Report the malaria status.
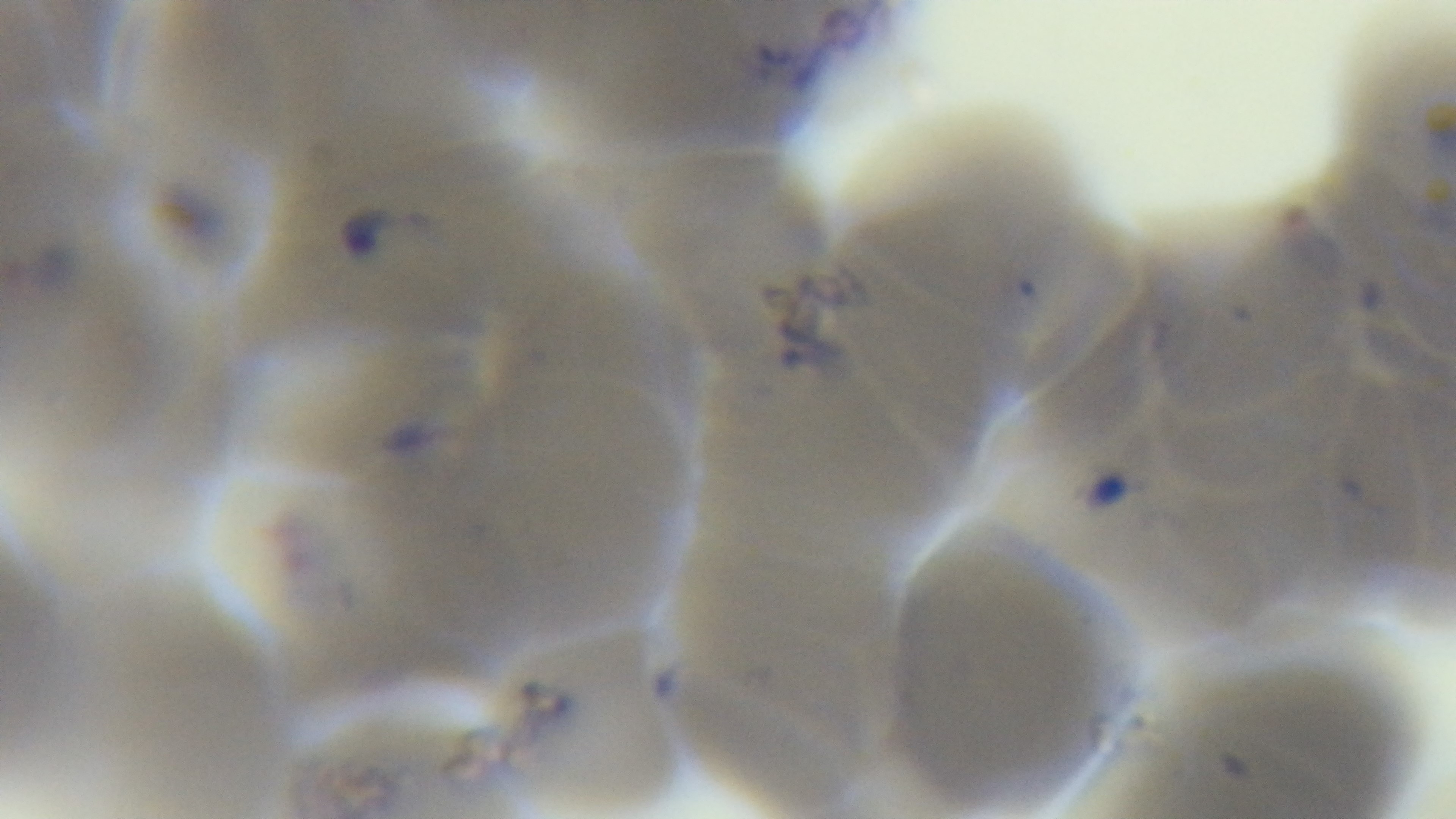

Positive.

Giemsa stain. Photomicrograph. Preparation: thin smear. 100x oil-immersion objective. Mounted 4K digital camera. Single field of view.